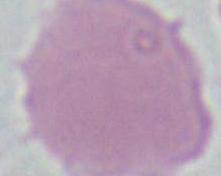
A red blood cell is shown. Micrograph. 1000x magnification.